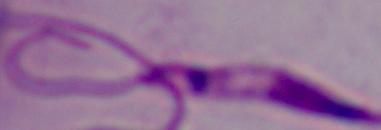 1000x magnification. A Leishmania parasite is shown. Micrograph.